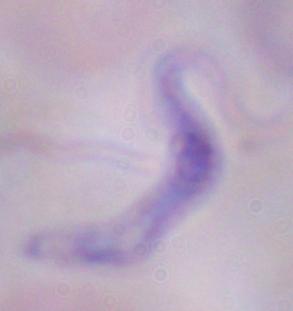
Captured at 1000x magnification. Micrograph. A trypanosome is seen.